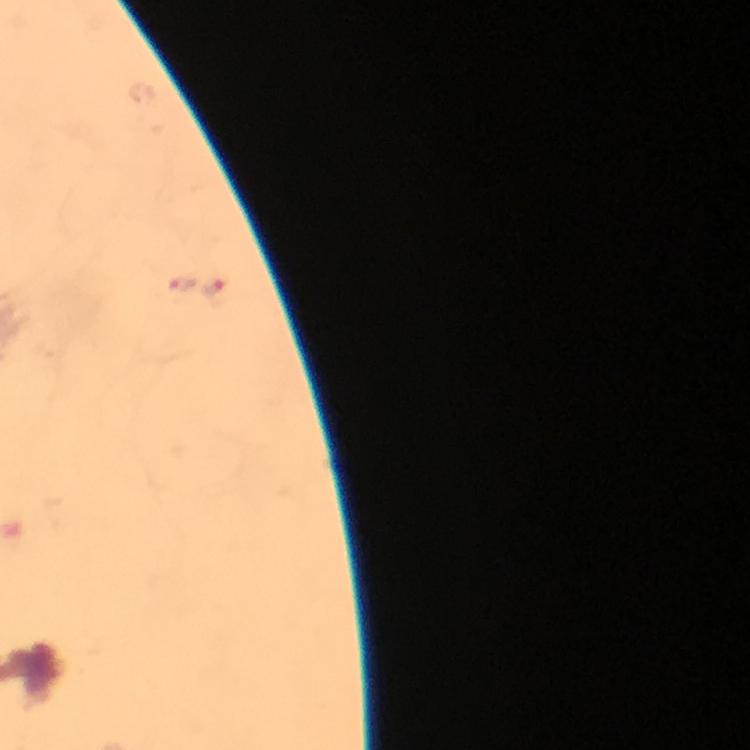
stain = Giemsa
immersion oil = used
Plasmodium parasite locations = approximate centers as [x, y] in pixels: [177, 285], [217, 290]
capture = smartphone photograph through a microscope
magnification = 100x
preparation = thick smear
image size = 750×750 pixels
context = from a malaria diagnostic workup
cropped from = one field of view